Give the extent of all uninfected red blood cells.
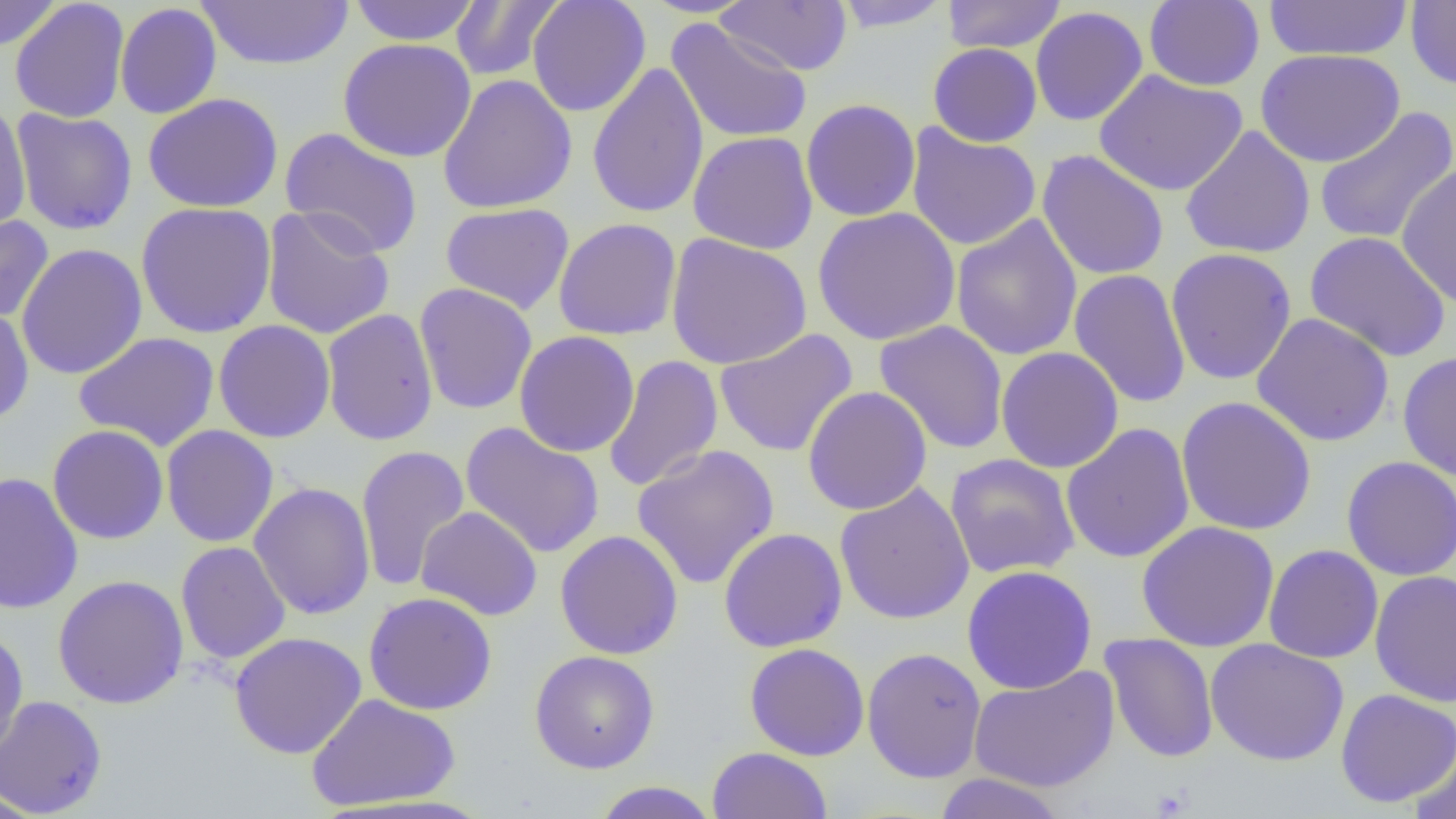
Approximate bounding boxes as [x1, y1, x2, y2] in pixels.
Uninfected red blood cells: [0, 0, 63, 51], [198, 0, 354, 70], [348, 0, 482, 45], [450, 0, 565, 81], [527, 0, 651, 117], [638, 0, 760, 18], [832, 0, 954, 33], [942, 0, 1066, 54], [1144, 0, 1265, 91], [10, 1, 130, 123], [718, 1, 851, 76], [1262, 1, 1413, 61], [1406, 1, 1456, 90], [114, 3, 222, 119], [1030, 6, 1148, 126], [665, 18, 813, 144], [338, 38, 476, 162], [928, 43, 1042, 147], [1255, 48, 1406, 168], [587, 61, 709, 220], [1094, 69, 1248, 197], [437, 74, 577, 214], [143, 93, 283, 213], [801, 98, 921, 222], [0, 102, 31, 236], [1313, 106, 1456, 246], [11, 107, 138, 236], [800, 109, 1039, 230], [906, 123, 1041, 251], [1179, 125, 1315, 259], [279, 127, 424, 257], [688, 131, 819, 254], [1036, 149, 1169, 281], [1396, 162, 1456, 310], [135, 201, 276, 339], [440, 202, 575, 315], [261, 205, 395, 340], [812, 206, 961, 346], [0, 215, 54, 323], [950, 215, 1083, 360], [553, 217, 682, 340], [1305, 231, 1451, 362], [665, 233, 812, 370], [15, 243, 148, 380], [1165, 247, 1297, 385], [1069, 269, 1192, 409], [413, 283, 538, 415], [0, 304, 34, 425], [321, 308, 438, 446], [1251, 313, 1394, 447], [213, 320, 336, 443], [874, 320, 1009, 455], [714, 328, 858, 457], [514, 330, 640, 457], [74, 331, 220, 451], [995, 346, 1124, 473], [1397, 351, 1456, 481], [603, 354, 723, 492], [802, 386, 932, 515], [1176, 395, 1316, 536], [461, 422, 605, 558], [1060, 422, 1195, 564], [47, 424, 169, 544], [161, 424, 279, 547], [355, 444, 470, 592], [631, 444, 780, 589], [945, 453, 1080, 579], [1341, 456, 1456, 581], [0, 471, 84, 615], [834, 481, 975, 625], [249, 482, 375, 619], [416, 506, 542, 621], [1137, 521, 1279, 652], [718, 527, 848, 653], [555, 530, 683, 660], [175, 541, 290, 665], [1264, 544, 1383, 664], [961, 564, 1097, 694], [1370, 569, 1456, 707], [52, 574, 189, 709], [363, 592, 497, 715], [0, 627, 29, 760], [229, 631, 367, 759], [1100, 633, 1219, 763], [1206, 639, 1349, 766], [744, 643, 870, 761], [861, 646, 987, 783], [530, 650, 660, 774], [968, 665, 1120, 793], [1334, 689, 1456, 807], [306, 693, 461, 811], [0, 695, 108, 817], [1409, 739, 1456, 819], [707, 747, 833, 819], [932, 773, 1069, 818], [590, 781, 720, 818], [0, 789, 45, 818].

Slide-level diagnosis: negative for blood parasites. 1000x magnification. Optical microscopy. Image is 1456×819 pixels. Thin blood smear. One field of a larger specimen.